Assess the morphology of the erythrocytes.
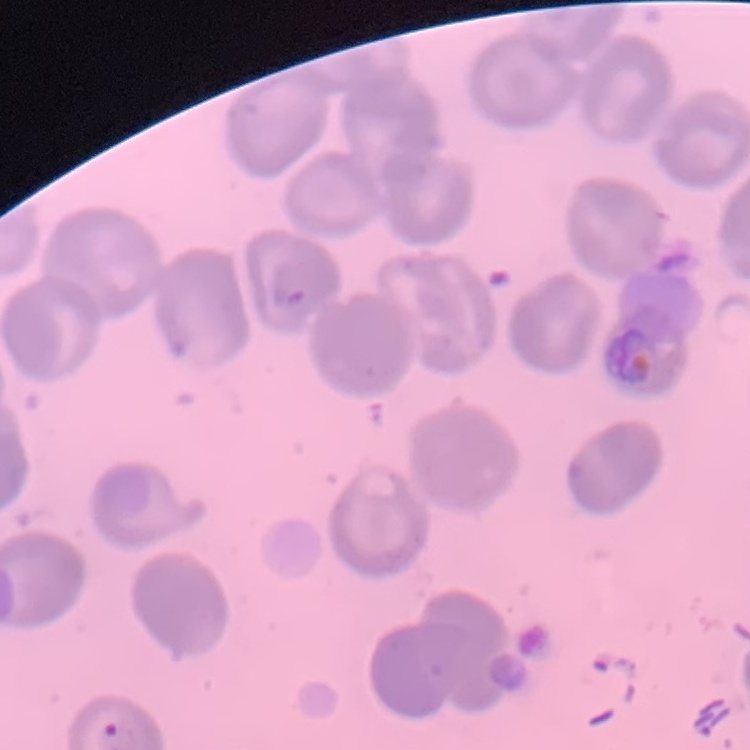
They show no rouleaux formation.

One tile cut from a larger photomicrograph. Thin peripheral smear. Field's or Giemsa stain.